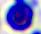
magnification = 400x
modality = micrograph
identification = leukocyte